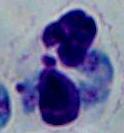 Micrograph. Captured at 1000x magnification. A leukocyte is shown.